Report the malaria status of this cell.
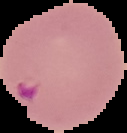

Parasitized.

Cell region segmented out of the field of view; the surrounding area is masked to black. Image is 127×133 pixels. From a thin blood film.